Point out cells.
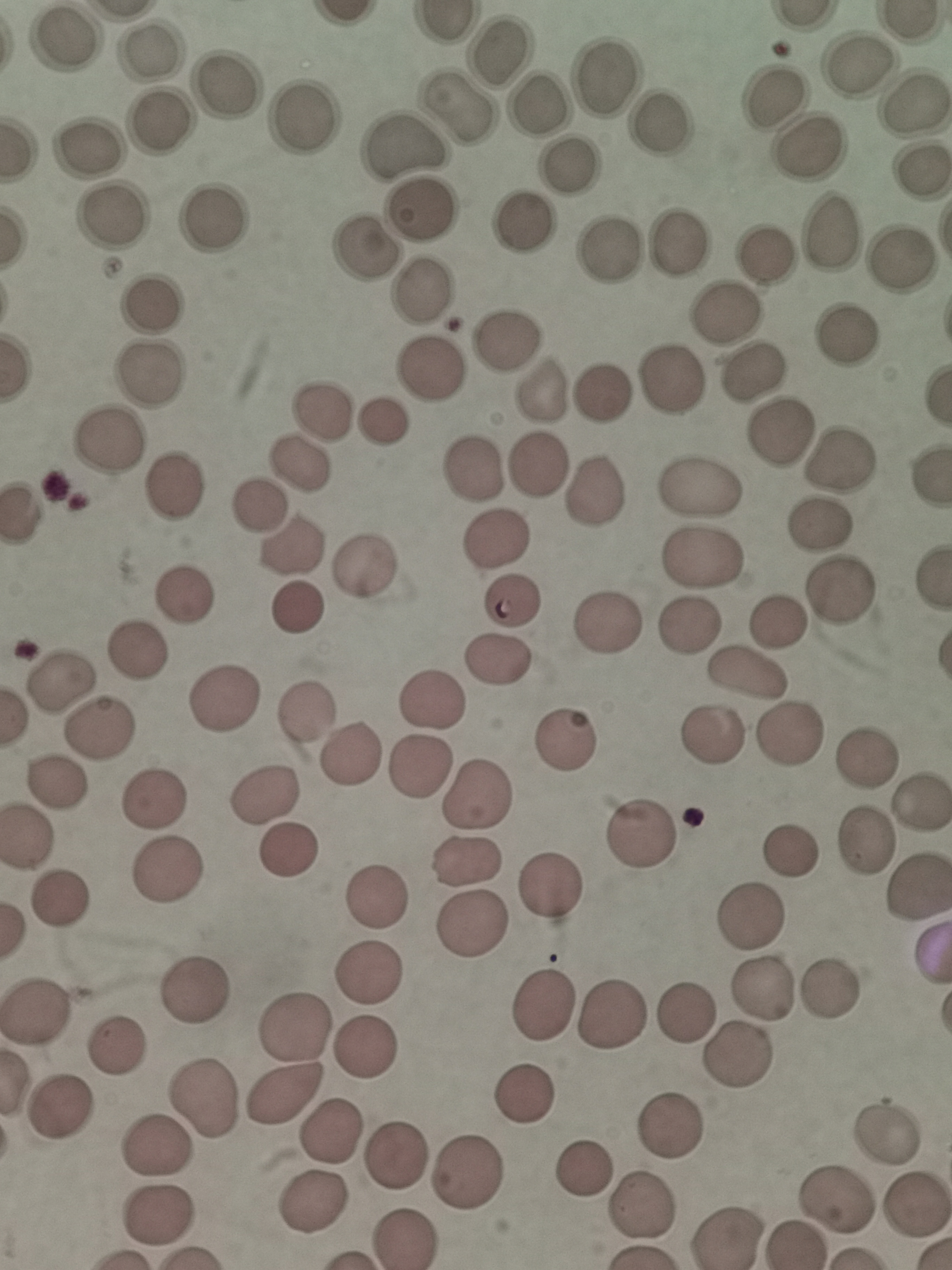
Approximate centers as (x, y) in pixels.
Cells: (61, 42), (153, 50), (502, 54), (862, 67), (603, 79), (228, 84), (769, 90), (534, 107), (912, 107), (455, 112), (302, 117), (159, 122), (662, 124), (404, 146), (88, 148), (806, 153), (570, 164), (918, 170), (423, 212), (108, 218), (520, 224), (216, 228), (826, 231), (675, 243), (364, 247), (608, 251), (769, 253), (900, 262), (426, 287), (145, 302), (727, 314), (507, 336), (841, 342), (427, 367), (148, 374), (753, 378), (671, 381), (542, 387), (602, 387), (320, 413), (380, 422), (776, 432), (102, 445), (537, 461), (839, 461), (299, 464), (473, 469), (172, 482), (594, 489), (701, 489), (256, 502), (816, 525), (496, 539), (292, 549), (703, 556), (363, 563), (837, 590), (188, 591), (510, 600), (297, 608), (608, 620), (776, 620), (688, 624), (139, 649), (501, 662), (746, 676), (63, 677), (220, 694), (428, 704), (305, 715), (101, 725), (716, 731), (788, 734), (566, 735), (351, 753), (868, 757), (421, 769), (59, 781), (264, 794), (480, 797), (156, 800), (921, 803), (645, 834), (864, 840), (287, 850), (792, 852), (468, 864), (169, 872), (555, 885), (375, 893), (63, 896), (752, 917), (473, 930), (369, 978), (193, 987), (760, 988), (828, 989), (544, 1003), (39, 1009), (686, 1011), (616, 1015), (294, 1028), (364, 1049), (116, 1051), (735, 1059), (526, 1094), (200, 1098), (283, 1098), (60, 1108), (673, 1122), (333, 1130), (887, 1134), (156, 1146), (398, 1152), (582, 1166), (470, 1172), (315, 1200), (832, 1202), (916, 1206), (640, 1207), (157, 1218), (404, 1237), (730, 1238).

Thin blood smear. Image is 952×1270 pixels. Giemsa stain. Acquired by smartphone through the microscope eyepiece. Single field of view.